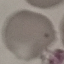

Result: no malaria parasites seen. Acquired by smartphone through the microscope eyepiece. Automatically extracted cell patch, resized to 64 × 64 pixels. Thin blood film. Giemsa stain.